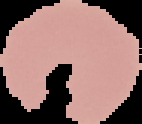
The area outside the segmented cell region is set to black. Image is 142×124 pixels. From a thin blood smear. Result: no Plasmodium parasites detected.